State which cell type is depicted.
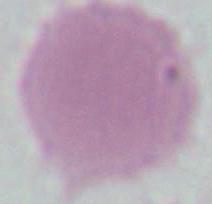
This is an erythrocyte.

Captured at 1000x magnification. Photomicrograph.